Classify this cell by malaria status.
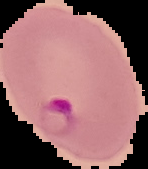

It is parasitized.

Cell region segmented out of the field of view; the surrounding area is masked to black. From a thin blood film. Image is 148×169 pixels.